Classify this cell by malaria status.
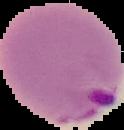

It is parasitized.

image size = 124×130 pixels
image type = segmented cell region with the area outside set to black
preparation = thin blood smear